Give the position of every leukocyte visible.
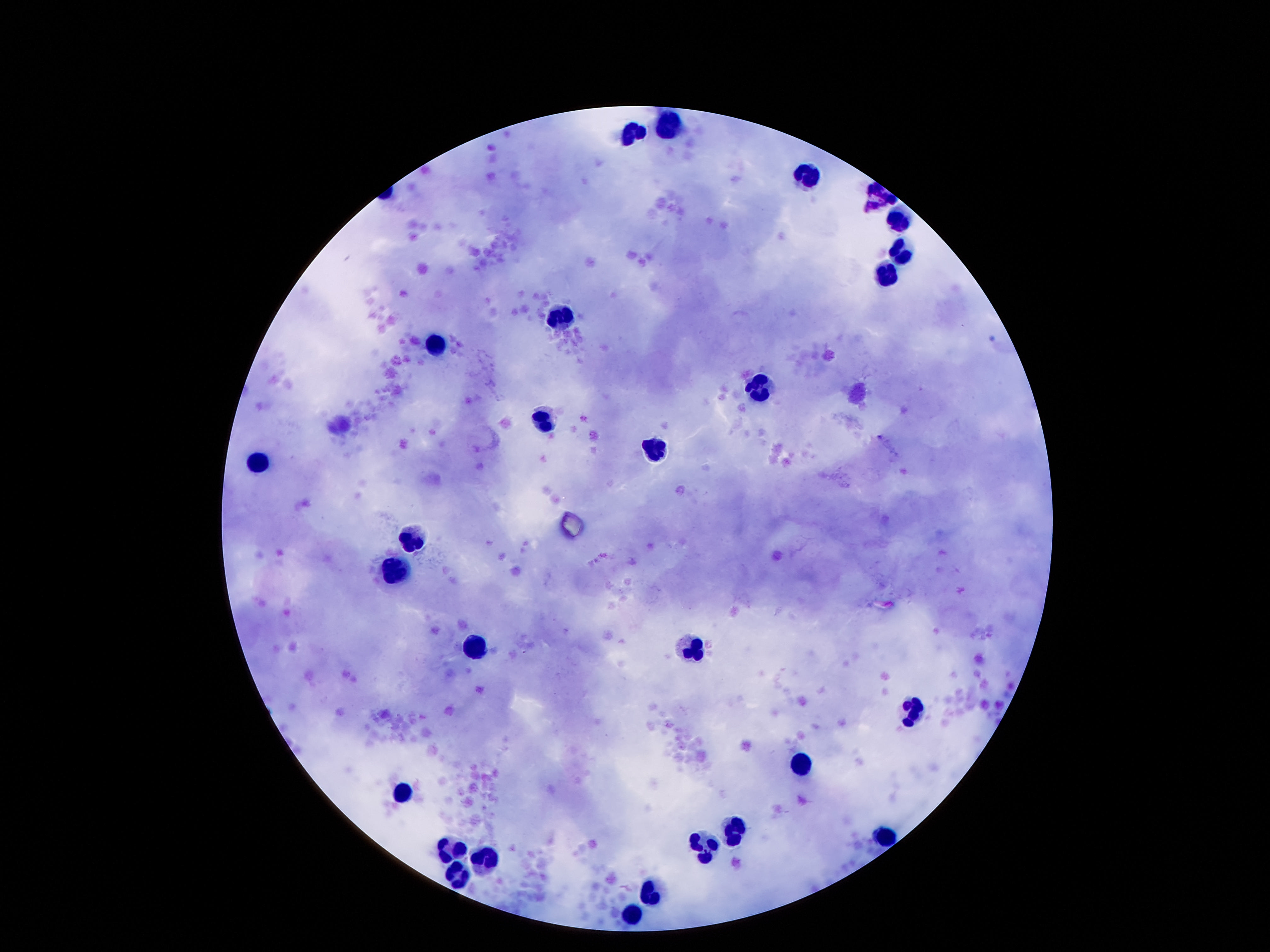

Approximate centers as [x, y] in pixels.
Leukocytes: [673, 128], [628, 134], [808, 175], [880, 197], [898, 224], [898, 251], [882, 277], [560, 312], [433, 343], [757, 388], [544, 419], [654, 447], [261, 464], [411, 539], [398, 568], [702, 646], [474, 650], [913, 707], [802, 765], [402, 793], [734, 828], [882, 836], [706, 847], [452, 849], [488, 861], [458, 873], [654, 892], [634, 914].

100x magnification. Thick blood film. Giemsa-stained preparation. Image is 1270×952 pixels. Patient malaria status: not infected. Smartphone photograph taken through the microscope eyepiece. Single field of view.